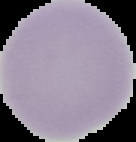
Image is 136×142 pixels. Segmented cell region on a black background. From a thin blood smear. Result: no Plasmodium parasites detected.